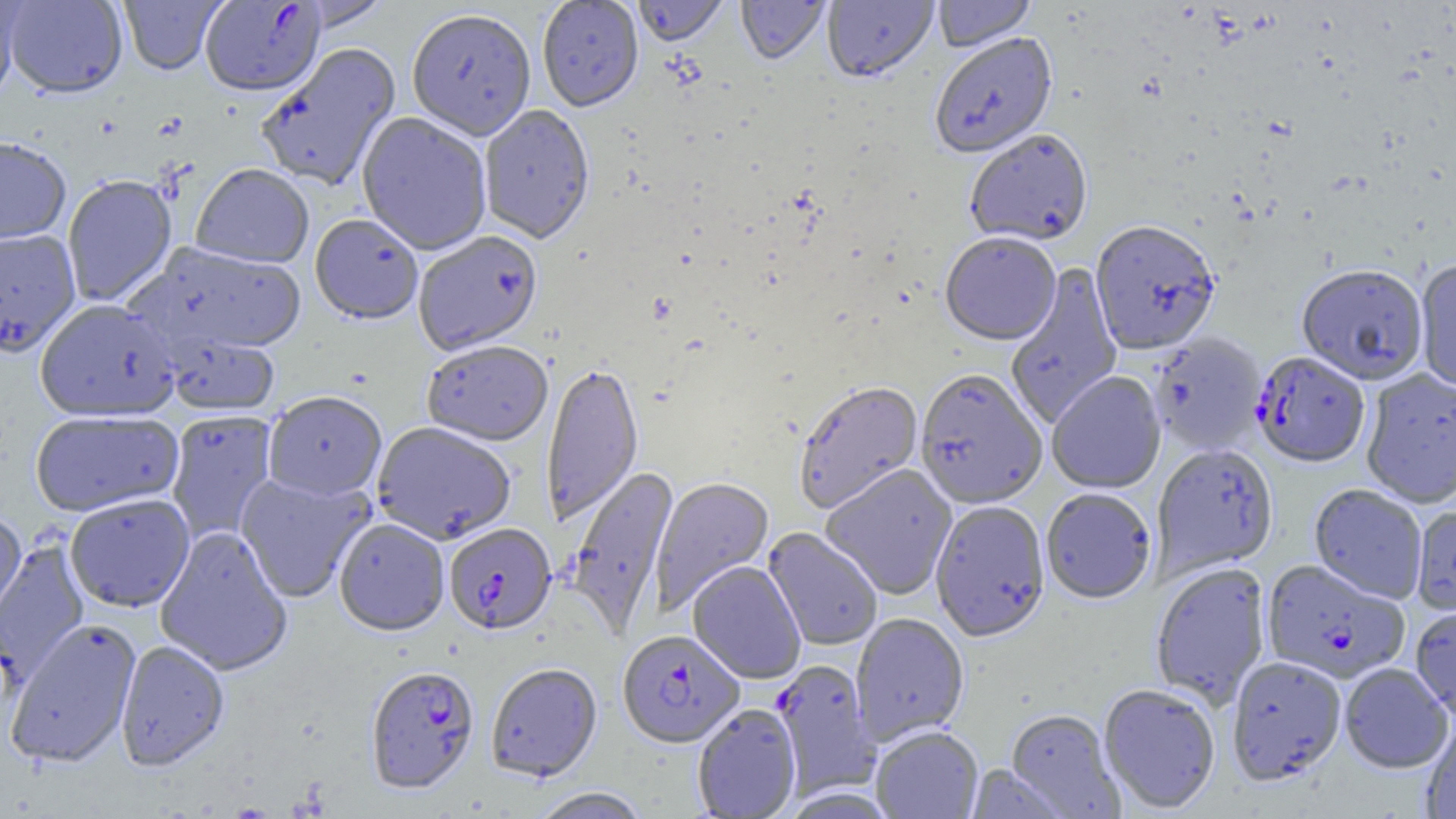
Summary:
  - Coordinate format: approximate bounding boxes as named x1/y1/x2/y2 corners in pixels
  - Plasmodium falciparum-infected red blood cell locations (subset): (x1=200, y1=1, x2=325, y2=98), (x1=1251, y1=353, x2=1370, y2=470), (x1=444, y1=525, x2=556, y2=637), (x1=1261, y1=560, x2=1411, y2=686), (x1=617, y1=630, x2=744, y2=749), (x1=365, y1=668, x2=480, y2=798)
  - Uninfected red blood cell locations (subset): (x1=0, y1=0, x2=29, y2=104), (x1=3, y1=0, x2=128, y2=101), (x1=119, y1=0, x2=227, y2=76), (x1=537, y1=0, x2=644, y2=114), (x1=633, y1=0, x2=728, y2=47), (x1=822, y1=0, x2=938, y2=85), (x1=932, y1=0, x2=1036, y2=53), (x1=291, y1=1, x2=393, y2=32), (x1=736, y1=1, x2=832, y2=67), (x1=407, y1=10, x2=536, y2=142), (x1=929, y1=34, x2=1059, y2=160), (x1=255, y1=43, x2=401, y2=193), (x1=478, y1=106, x2=595, y2=246), (x1=356, y1=113, x2=492, y2=257), (x1=965, y1=132, x2=1093, y2=248), (x1=0, y1=137, x2=70, y2=247), (x1=190, y1=165, x2=314, y2=270), (x1=62, y1=176, x2=177, y2=308), (x1=309, y1=216, x2=423, y2=327), (x1=1090, y1=223, x2=1220, y2=357), (x1=0, y1=230, x2=81, y2=360), (x1=413, y1=233, x2=543, y2=357), (x1=940, y1=235, x2=1062, y2=347), (x1=128, y1=242, x2=308, y2=359), (x1=1414, y1=261, x2=1456, y2=393), (x1=1005, y1=262, x2=1123, y2=428), (x1=1297, y1=267, x2=1429, y2=386), (x1=34, y1=301, x2=181, y2=423), (x1=163, y1=333, x2=279, y2=417), (x1=1150, y1=334, x2=1266, y2=456), (x1=422, y1=342, x2=554, y2=449), (x1=541, y1=364, x2=644, y2=526), (x1=1361, y1=369, x2=1456, y2=510), (x1=915, y1=371, x2=1047, y2=511), (x1=1047, y1=372, x2=1166, y2=495), (x1=793, y1=383, x2=924, y2=515), (x1=264, y1=393, x2=387, y2=502), (x1=30, y1=410, x2=184, y2=519), (x1=165, y1=411, x2=279, y2=543), (x1=372, y1=424, x2=516, y2=546), (x1=1152, y1=446, x2=1278, y2=579), (x1=820, y1=464, x2=958, y2=601), (x1=567, y1=466, x2=680, y2=639), (x1=235, y1=473, x2=376, y2=603), (x1=650, y1=476, x2=774, y2=615), (x1=1309, y1=485, x2=1427, y2=604), (x1=1041, y1=489, x2=1157, y2=606), (x1=65, y1=495, x2=195, y2=613), (x1=930, y1=502, x2=1051, y2=644), (x1=0, y1=513, x2=28, y2=629), (x1=334, y1=520, x2=449, y2=638), (x1=155, y1=527, x2=293, y2=678), (x1=763, y1=528, x2=883, y2=652), (x1=0, y1=540, x2=91, y2=693), (x1=688, y1=562, x2=805, y2=685), (x1=1150, y1=563, x2=1272, y2=709), (x1=1410, y1=606, x2=1456, y2=722), (x1=851, y1=614, x2=969, y2=746), (x1=4, y1=619, x2=142, y2=770), (x1=116, y1=641, x2=229, y2=773), (x1=1226, y1=657, x2=1348, y2=787), (x1=1340, y1=663, x2=1453, y2=774), (x1=485, y1=664, x2=602, y2=783), (x1=1098, y1=685, x2=1220, y2=815), (x1=692, y1=705, x2=802, y2=819), (x1=1005, y1=710, x2=1126, y2=818), (x1=1421, y1=721, x2=1456, y2=819), (x1=871, y1=726, x2=984, y2=819), (x1=964, y1=766, x2=1070, y2=818), (x1=529, y1=788, x2=651, y2=819)
  - Slide-level diagnosis: Plasmodium falciparum
  - Field of view: one of a larger specimen
  - Modality: light microscopy
  - Preparation: thin blood smear
  - Image size: 1456×819 pixels
  - Magnification: 1000x